Classify this cell by malaria status.
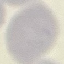

It is uninfected.

stain = Giemsa
capture = smartphone camera at the microscope eyepiece
preparation = thin smear
image type = automatically extracted cell patch, resized to 64 × 64 pixels